Report the malaria status of this cell.
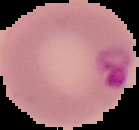

Parasitized.

preparation: thin blood film
image_size: 139×130 pixels
image_type: segmented cell region with the area outside set to black